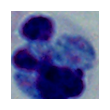 A leukocyte is seen. Micrograph. 1000x magnification.